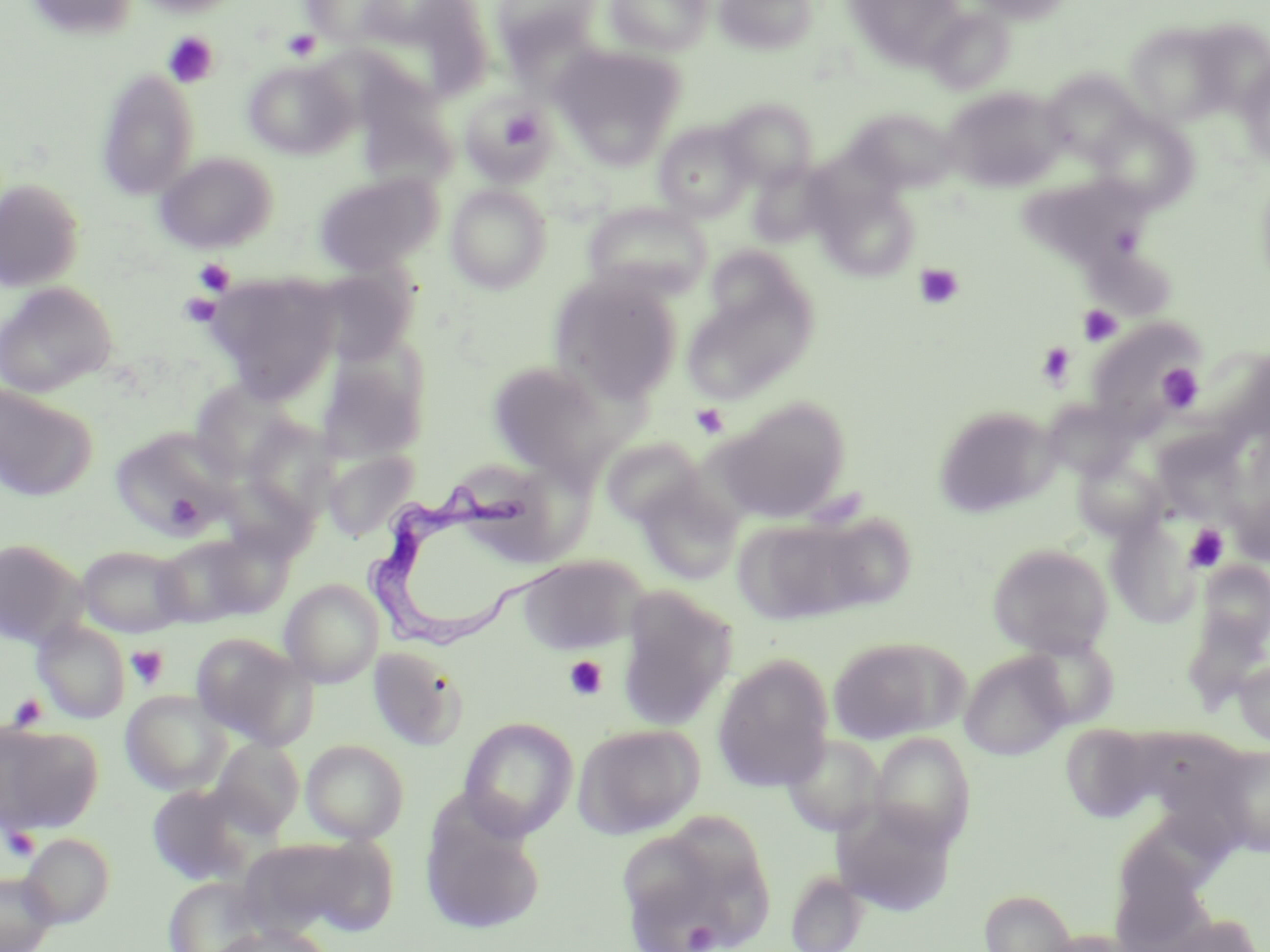

Summary:
  - Coordinate format: approximate bounding boxes as [x1, y1, x2, y2] in pixels
  - Platelet locations: [282, 29, 321, 61], [162, 32, 219, 88], [501, 110, 543, 152], [193, 258, 235, 295], [914, 263, 964, 310], [178, 292, 222, 328], [1077, 304, 1122, 347], [1037, 342, 1076, 388], [1156, 364, 1204, 413], [691, 403, 729, 439], [1184, 524, 1229, 571], [125, 644, 169, 690], [564, 655, 608, 701], [7, 693, 47, 730], [3, 827, 41, 860], [685, 922, 719, 951]
  - Uninfected red blood cell locations: [25, 0, 139, 41], [133, 0, 244, 17], [300, 0, 414, 49], [364, 0, 493, 102], [491, 0, 603, 69], [604, 0, 712, 55], [714, 0, 819, 55], [843, 0, 966, 68], [968, 0, 1073, 24], [926, 8, 1014, 95], [1188, 19, 1270, 116], [1123, 21, 1234, 126], [551, 45, 685, 166], [244, 59, 357, 159], [1237, 61, 1270, 167], [96, 69, 200, 200], [1041, 69, 1144, 163], [942, 87, 1065, 191], [460, 94, 554, 182], [718, 98, 817, 189], [847, 108, 960, 194], [1090, 109, 1198, 213], [654, 120, 755, 222], [733, 120, 826, 232], [155, 151, 277, 253], [748, 162, 835, 248], [313, 172, 442, 275], [1017, 174, 1150, 269], [0, 178, 86, 291], [816, 181, 920, 280], [445, 184, 552, 293], [583, 203, 712, 300], [705, 246, 809, 333], [1085, 253, 1179, 315], [308, 266, 417, 366], [207, 272, 342, 400], [550, 273, 683, 403], [0, 282, 116, 398], [682, 285, 814, 404], [1086, 317, 1203, 433], [315, 360, 426, 466], [487, 360, 620, 479], [187, 380, 302, 482], [0, 384, 97, 502], [1040, 398, 1137, 481], [717, 399, 850, 522], [933, 405, 1057, 518], [241, 418, 341, 527], [111, 427, 239, 537], [1152, 430, 1249, 523], [601, 436, 706, 527], [323, 448, 420, 541], [1072, 452, 1167, 541], [635, 475, 743, 585], [811, 513, 917, 611], [732, 516, 870, 627], [1106, 516, 1201, 627], [153, 534, 262, 627], [0, 538, 86, 647], [988, 542, 1114, 658], [77, 545, 190, 638], [517, 555, 646, 654], [1197, 560, 1270, 654], [280, 579, 383, 687], [615, 587, 736, 732], [1181, 612, 1269, 714], [32, 618, 130, 724], [191, 632, 316, 748], [827, 635, 967, 745], [1020, 635, 1119, 729], [367, 646, 468, 752], [959, 651, 1072, 760], [712, 654, 834, 792], [1233, 657, 1270, 747], [120, 689, 232, 795], [458, 716, 578, 840], [0, 722, 102, 833], [1060, 722, 1162, 823], [572, 723, 704, 839], [1142, 726, 1251, 803], [869, 732, 975, 850], [780, 733, 885, 838], [211, 737, 304, 836], [300, 739, 409, 843], [1214, 745, 1270, 856], [146, 784, 252, 886], [832, 803, 958, 915], [420, 813, 544, 936], [617, 822, 773, 952], [20, 833, 116, 928], [240, 836, 392, 938], [785, 870, 869, 952], [0, 871, 58, 952], [164, 877, 263, 952], [979, 888, 1077, 952], [213, 923, 334, 952]
  - Trypanosoma brucei locations: [375, 479, 541, 649]
  - Slide-level diagnosis: Trypanosoma brucei
  - Image size: 1270×952 pixels
  - Preparation: thin blood film
  - Stain: May-Grünwald-Giemsa
  - Modality: light microscopy
  - Magnification: 1000x
  - Field of view: one of a larger specimen